Name the parasite shown.
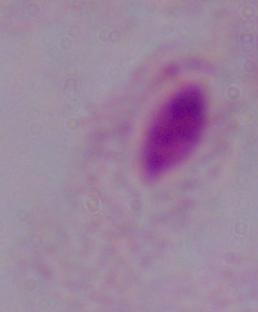

This is a trichomonad.

Summary:
  - Magnification: 1000x
  - Modality: photomicrograph